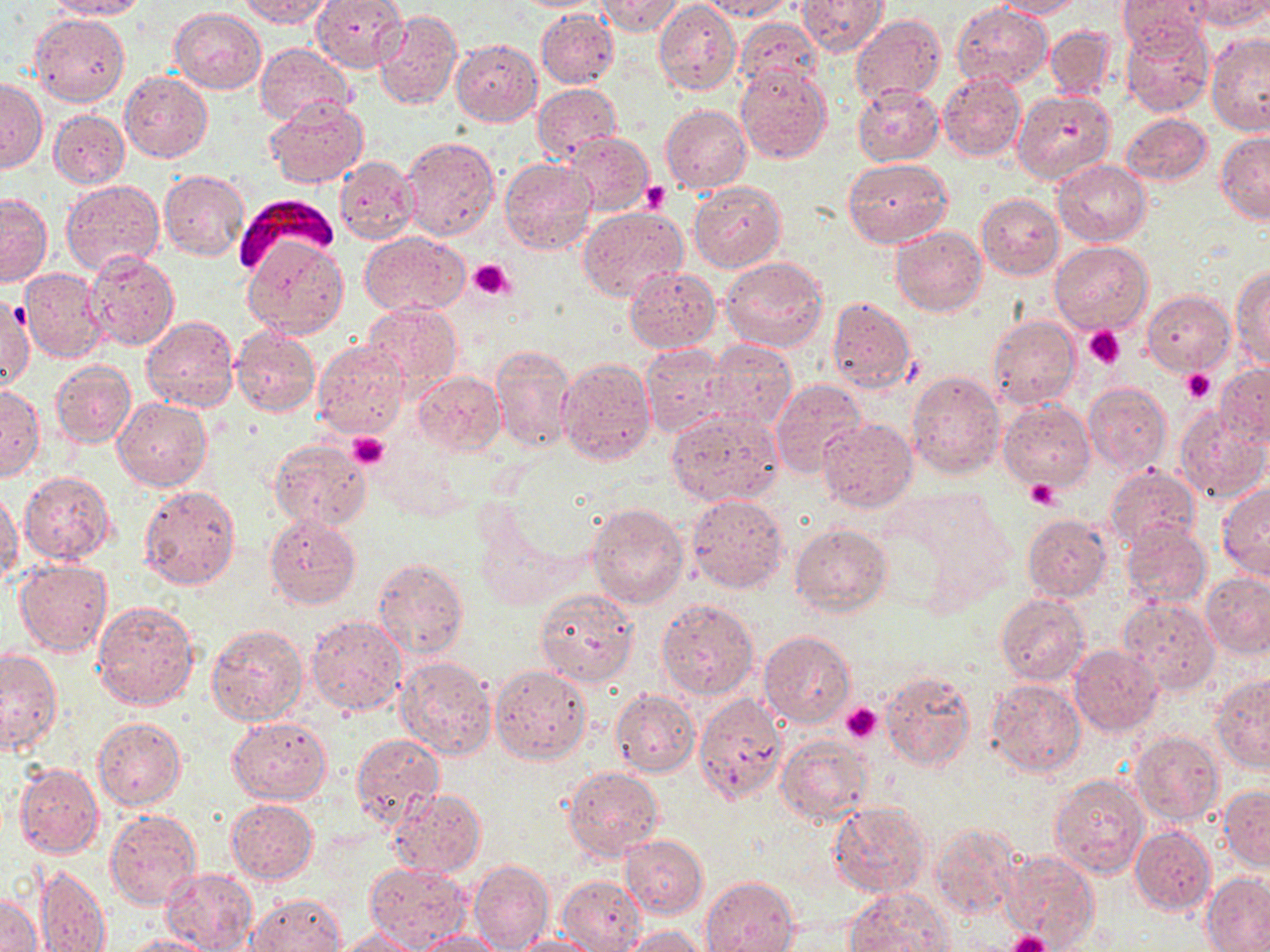

slide-level diagnosis = Plasmodium falciparum
modality = optical microscopy
stain = May-Grünwald-Giemsa
field of view = one of a larger specimen
Plasmodium falciparum-infected red blood cell locations = approximate bounding boxes as [x1, y1, x2, y2] in pixels: [235, 196, 337, 279]
preparation = thin blood smear
magnification = 1000x
image size = 1270×952 pixels
platelet locations = approximate bounding boxes as [x1, y1, x2, y2] in pixels: [640, 182, 670, 212], [468, 260, 514, 299], [1084, 325, 1126, 365], [1181, 368, 1215, 404], [346, 433, 389, 470], [1026, 481, 1059, 509], [840, 703, 883, 744], [1006, 931, 1052, 952]
uninfected red blood cell locations = approximate bounding boxes as [x1, y1, x2, y2] in pixels: [45, 0, 145, 20], [241, 0, 336, 27], [312, 0, 406, 70], [596, 0, 682, 37], [701, 0, 793, 21], [795, 0, 890, 57], [992, 0, 1084, 19], [1117, 0, 1214, 50], [1191, 0, 1270, 31], [654, 2, 742, 95], [952, 3, 1052, 90], [169, 9, 267, 94], [536, 9, 618, 88], [374, 10, 463, 109], [29, 13, 130, 106], [849, 14, 945, 103], [735, 17, 824, 98], [1121, 20, 1216, 117], [1045, 25, 1118, 101], [1207, 34, 1270, 135], [451, 39, 542, 127], [256, 43, 354, 125], [735, 63, 832, 162], [937, 71, 1025, 161], [121, 72, 212, 162], [0, 78, 45, 172], [852, 83, 944, 166], [533, 84, 620, 161], [1012, 89, 1117, 186], [265, 97, 368, 188], [661, 105, 752, 193], [49, 109, 129, 187], [1122, 113, 1212, 186], [1216, 132, 1270, 223], [567, 133, 651, 215], [402, 136, 498, 239], [335, 155, 419, 243], [500, 158, 596, 255], [843, 158, 951, 247], [1054, 159, 1150, 245], [158, 170, 248, 261], [60, 180, 166, 277], [689, 182, 786, 273], [1, 193, 52, 286], [976, 194, 1063, 279], [578, 208, 688, 301], [891, 226, 987, 316], [360, 232, 469, 317], [1052, 241, 1152, 333], [243, 243, 347, 337], [85, 250, 180, 350], [720, 256, 829, 353], [625, 267, 720, 352], [20, 268, 106, 363], [1232, 268, 1270, 368], [1142, 291, 1235, 374], [1, 292, 33, 393], [826, 296, 917, 392], [363, 303, 463, 391], [142, 315, 238, 412], [988, 316, 1079, 409], [231, 326, 320, 417], [313, 340, 409, 438], [703, 341, 797, 433], [492, 343, 575, 454], [640, 343, 730, 437], [557, 358, 656, 466], [51, 360, 136, 448], [1215, 363, 1270, 449], [413, 370, 506, 455], [907, 370, 1006, 479], [770, 379, 867, 481], [1084, 382, 1171, 475], [0, 386, 44, 481], [114, 398, 212, 491], [998, 402, 1093, 493], [1175, 406, 1269, 504], [666, 407, 784, 506], [817, 418, 916, 512], [267, 438, 373, 534], [1103, 465, 1200, 551], [20, 471, 115, 565], [1217, 483, 1270, 581], [138, 484, 241, 590], [0, 490, 22, 588], [686, 494, 788, 593], [588, 503, 689, 608], [474, 509, 563, 609], [264, 514, 360, 610], [1021, 514, 1111, 601], [1119, 521, 1211, 608], [789, 523, 893, 617], [373, 556, 469, 658], [14, 560, 112, 655], [1200, 571, 1270, 656], [534, 588, 640, 686], [995, 594, 1090, 685], [1118, 596, 1220, 694], [657, 598, 759, 698], [92, 599, 200, 711], [307, 612, 407, 715], [206, 623, 308, 727], [758, 630, 854, 728], [1069, 645, 1164, 736], [1, 647, 62, 756], [395, 655, 499, 761], [490, 667, 591, 764], [882, 669, 976, 770], [1212, 672, 1270, 773], [987, 677, 1086, 777], [610, 688, 699, 776], [693, 694, 787, 804], [228, 715, 331, 803], [92, 717, 186, 811], [1129, 731, 1223, 827], [351, 733, 443, 825], [776, 736, 872, 827], [15, 763, 103, 859], [564, 766, 664, 861], [1050, 772, 1151, 880], [1218, 786, 1270, 869], [388, 787, 486, 877], [227, 799, 317, 883], [829, 801, 931, 897], [104, 810, 201, 911], [931, 823, 1026, 923], [1130, 826, 1215, 915], [619, 834, 707, 918], [1003, 849, 1101, 950], [468, 859, 554, 952], [363, 861, 474, 950], [37, 864, 111, 952], [161, 867, 258, 952], [1202, 872, 1270, 951], [557, 874, 648, 952], [701, 876, 799, 952], [844, 887, 952, 952], [1, 890, 43, 952], [245, 893, 346, 952], [620, 925, 708, 951], [333, 927, 424, 951], [412, 930, 506, 950], [512, 933, 605, 952], [121, 934, 218, 952]